Identify the parasite.
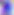

Toxoplasma gondii.

modality = photomicrograph
magnification = 400x